Draw a bounding box around every artifact (stain precipitate or debris).
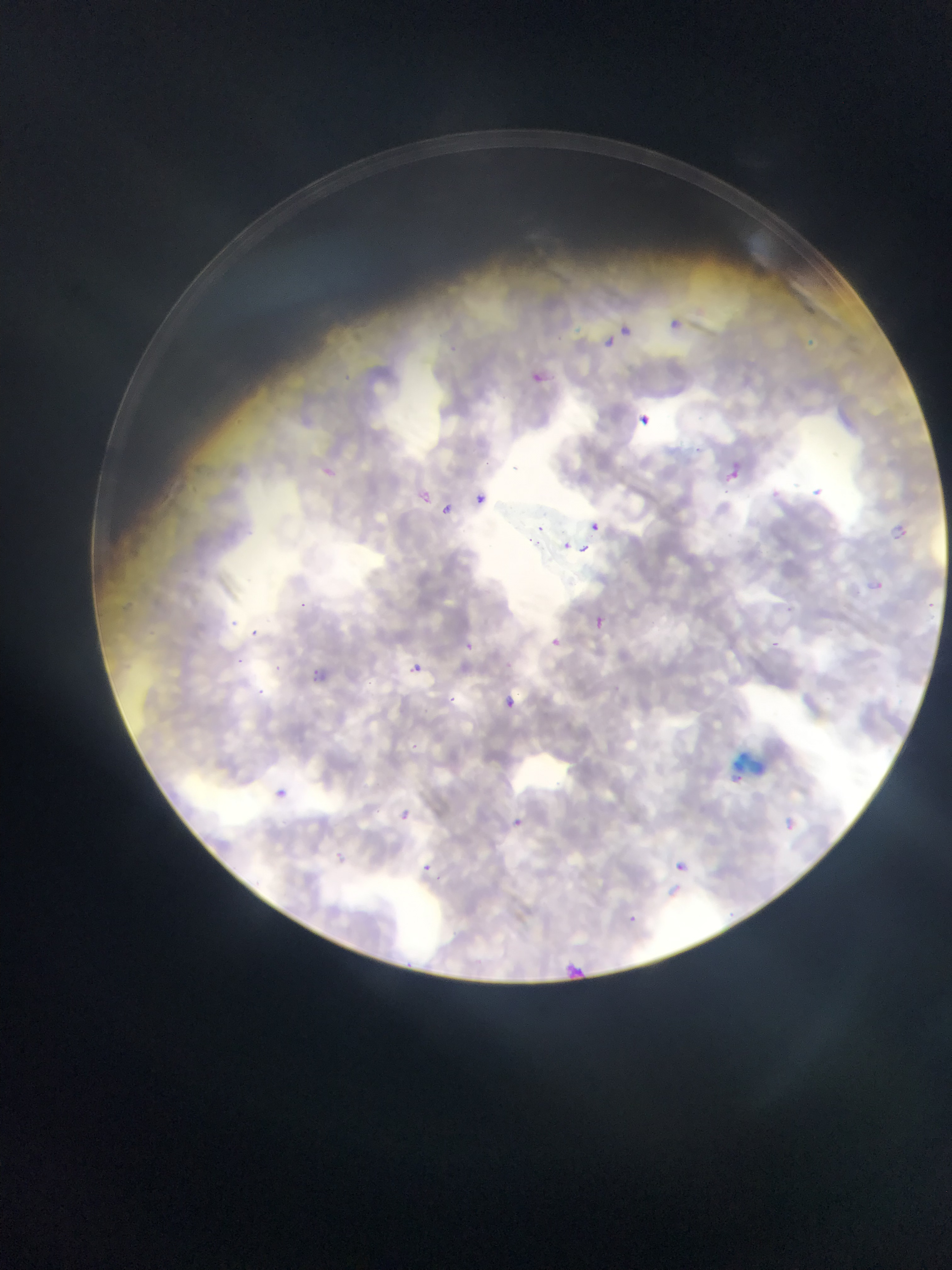
Approximate bounding boxes as left top right bottom in pixels.
Artifacts (stain precipitate or debris): 730 750 769 784.

Malaria parasite locations: 671 319 681 328; 621 324 633 339; 606 338 614 348; 808 339 816 350; 450 346 456 354; 343 374 352 381; 695 445 701 453; 512 466 520 473; 725 466 740 484; 814 484 826 495; 478 492 484 503; 443 504 454 515; 591 524 600 535; 891 525 910 541; 579 546 593 553; 786 608 794 613; 596 617 604 628; 253 628 261 637; 552 635 562 645; 465 644 472 652; 238 658 246 663; 274 666 283 671; 407 669 416 673; 506 694 518 710; 450 696 459 704; 276 789 287 799; 401 810 413 819; 514 820 522 828; 423 866 431 870; 631 914 636 922 | approximate x y pixel centers of objects too small to bound: 489 462; 726 492; 540 529; 530 539; 538 543; 566 546; 303 605; 235 623; 775 644; 416 667; 315 671; 316 679; 261 692. Mobile-phone photograph taken through the microscope. Thin blood film. Collected in Ghana. One field of view. Image is 952×1270 pixels.